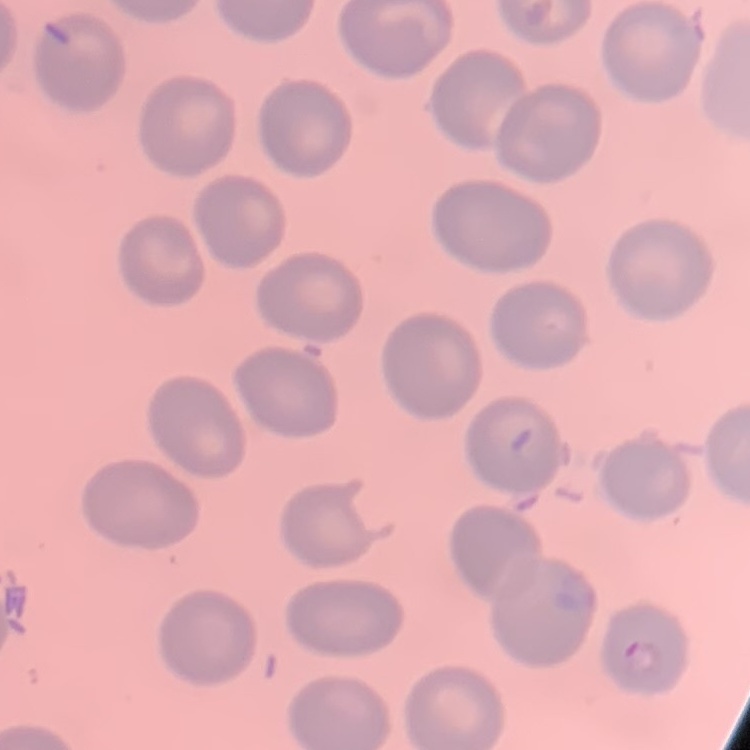
Summary:
  - Erythrocyte morphology: no rouleaux formation
  - Image type: one tile cut from a larger photomicrograph
  - Stain: Field's or Giemsa
  - Preparation: thin blood film